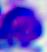 400x magnification. A leukocyte is shown. Photomicrograph.